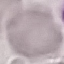

Result: negative for malaria parasites. Photographed with a smartphone camera at the microscope eyepiece. Thin smear of blood. Giemsa stain. Automatically extracted cell patch, resized to 64 × 64 pixels.